Locate every Plasmodium falciparum-infected red blood cell.
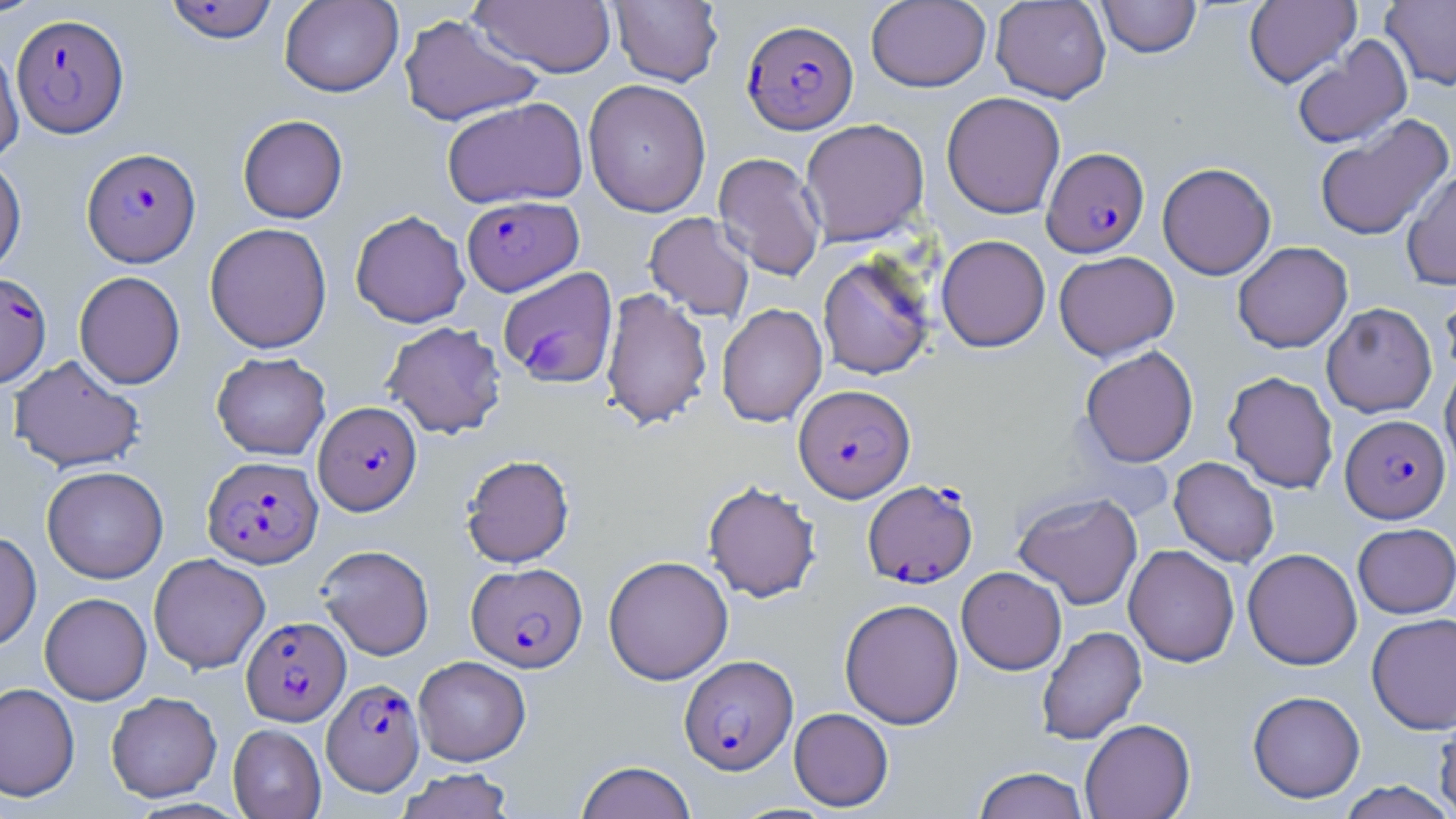
Approximate bounding boxes as named x1/y1/x2/y2 corners in pixels.
Plasmodium falciparum-infected red blood cells: (x1=161, y1=1, x2=280, y2=44), (x1=11, y1=13, x2=129, y2=138), (x1=742, y1=19, x2=857, y2=134), (x1=82, y1=147, x2=201, y2=266), (x1=1041, y1=147, x2=1149, y2=257), (x1=462, y1=195, x2=583, y2=296), (x1=0, y1=272, x2=52, y2=388), (x1=794, y1=384, x2=915, y2=501), (x1=313, y1=401, x2=421, y2=515), (x1=1341, y1=414, x2=1450, y2=523), (x1=202, y1=455, x2=323, y2=568), (x1=863, y1=480, x2=977, y2=587), (x1=467, y1=562, x2=587, y2=672), (x1=241, y1=616, x2=350, y2=726), (x1=679, y1=655, x2=798, y2=775), (x1=322, y1=679, x2=425, y2=795).

Summary:
  - Uninfected red blood cell locations: (x1=0, y1=0, x2=47, y2=18), (x1=279, y1=0, x2=404, y2=97), (x1=471, y1=0, x2=616, y2=78), (x1=609, y1=0, x2=723, y2=86), (x1=866, y1=0, x2=991, y2=92), (x1=990, y1=0, x2=1111, y2=103), (x1=1097, y1=0, x2=1201, y2=58), (x1=1244, y1=0, x2=1361, y2=87), (x1=1381, y1=1, x2=1456, y2=90), (x1=398, y1=13, x2=544, y2=126), (x1=1291, y1=35, x2=1413, y2=150), (x1=0, y1=39, x2=24, y2=163), (x1=583, y1=79, x2=712, y2=217), (x1=941, y1=92, x2=1066, y2=219), (x1=442, y1=97, x2=588, y2=209), (x1=237, y1=114, x2=348, y2=223), (x1=1314, y1=114, x2=1454, y2=241), (x1=800, y1=118, x2=929, y2=246), (x1=713, y1=152, x2=825, y2=281), (x1=0, y1=154, x2=26, y2=278), (x1=1157, y1=162, x2=1276, y2=279), (x1=1401, y1=169, x2=1456, y2=290), (x1=350, y1=209, x2=470, y2=328), (x1=644, y1=212, x2=755, y2=322), (x1=204, y1=222, x2=332, y2=353), (x1=936, y1=234, x2=1050, y2=352), (x1=1232, y1=241, x2=1353, y2=353), (x1=1053, y1=250, x2=1179, y2=360), (x1=817, y1=252, x2=936, y2=380), (x1=498, y1=266, x2=618, y2=388), (x1=74, y1=270, x2=185, y2=389), (x1=1439, y1=273, x2=1456, y2=382), (x1=600, y1=287, x2=712, y2=430), (x1=1321, y1=302, x2=1437, y2=418), (x1=716, y1=303, x2=827, y2=427), (x1=382, y1=320, x2=507, y2=438), (x1=1080, y1=346, x2=1198, y2=467), (x1=211, y1=352, x2=331, y2=460), (x1=8, y1=355, x2=146, y2=473), (x1=1440, y1=362, x2=1456, y2=479), (x1=1223, y1=371, x2=1339, y2=493), (x1=461, y1=454, x2=575, y2=567), (x1=1169, y1=457, x2=1279, y2=567), (x1=41, y1=465, x2=168, y2=583), (x1=703, y1=480, x2=821, y2=603), (x1=1013, y1=492, x2=1143, y2=609), (x1=1352, y1=522, x2=1456, y2=618), (x1=0, y1=531, x2=41, y2=651), (x1=316, y1=544, x2=435, y2=660), (x1=1124, y1=544, x2=1240, y2=667), (x1=1242, y1=548, x2=1362, y2=670), (x1=149, y1=553, x2=270, y2=673), (x1=603, y1=555, x2=733, y2=684), (x1=956, y1=566, x2=1067, y2=675), (x1=40, y1=592, x2=152, y2=705), (x1=839, y1=598, x2=964, y2=729), (x1=1367, y1=612, x2=1456, y2=734), (x1=1036, y1=626, x2=1147, y2=745), (x1=413, y1=656, x2=531, y2=765), (x1=0, y1=683, x2=80, y2=801), (x1=1247, y1=690, x2=1365, y2=803), (x1=106, y1=691, x2=222, y2=802), (x1=789, y1=707, x2=894, y2=811), (x1=1434, y1=708, x2=1456, y2=817), (x1=1080, y1=718, x2=1195, y2=819), (x1=227, y1=724, x2=326, y2=819), (x1=575, y1=761, x2=697, y2=819), (x1=973, y1=767, x2=1090, y2=819), (x1=396, y1=768, x2=516, y2=819), (x1=1335, y1=781, x2=1455, y2=818)
  - Slide-level diagnosis: Plasmodium falciparum
  - Image size: 1456×819 pixels
  - Preparation: thin blood smear
  - Modality: optical microscopy
  - Stain: May-Grünwald-Giemsa
  - Magnification: 1000x
  - Field of view: single